Outline each Plasmodium malariae-infected red blood cell.
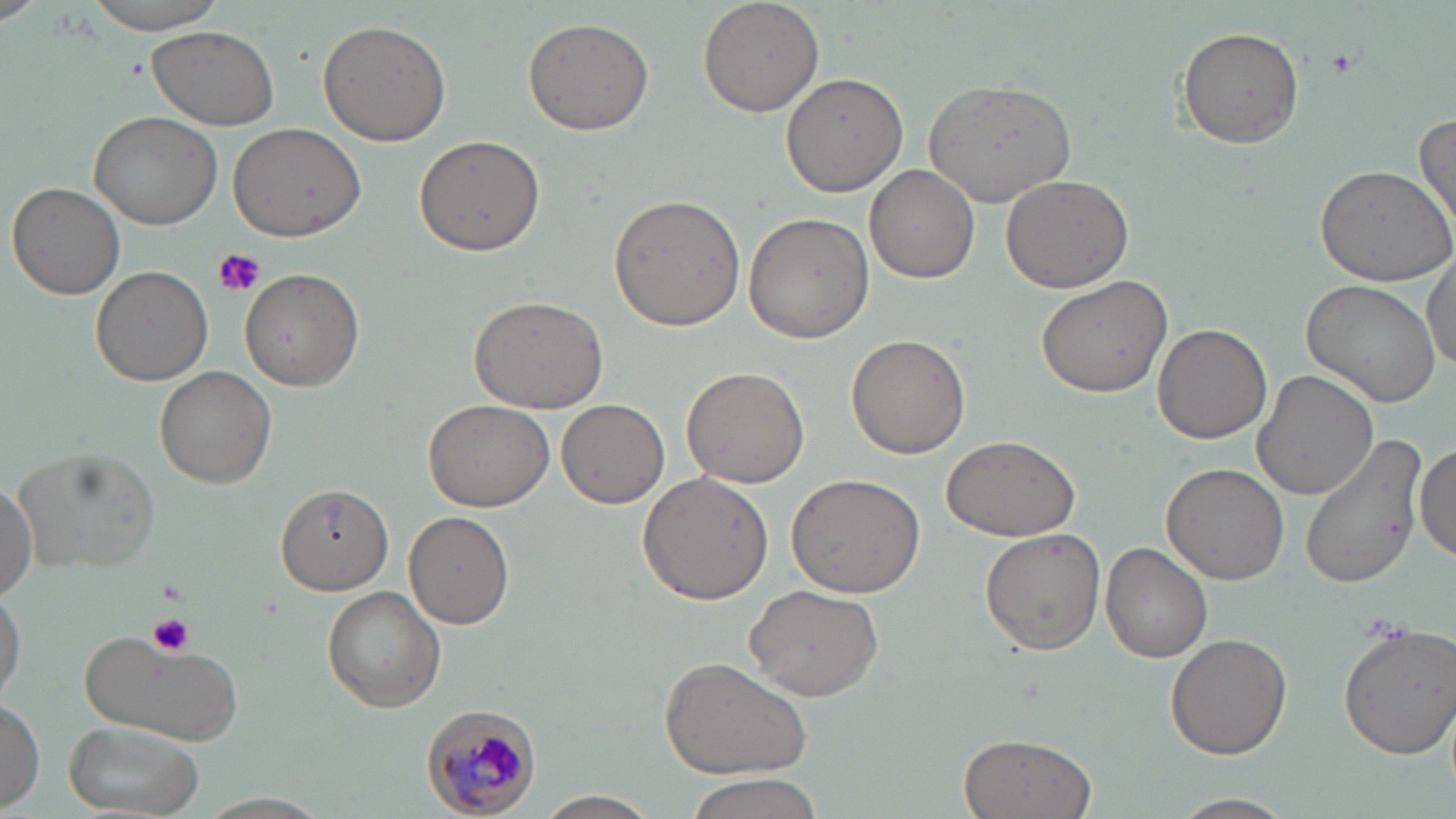
Approximate bounding boxes as [x1, y1, x2, y2] in pixels.
Plasmodium malariae-infected red blood cells: [421, 707, 544, 818].

Uninfected red blood cell locations: [79, 0, 231, 34], [697, 0, 825, 116], [521, 17, 655, 136], [318, 19, 451, 146], [146, 26, 281, 130], [1177, 27, 1304, 149], [782, 70, 909, 197], [924, 79, 1080, 205], [89, 108, 224, 228], [1412, 111, 1456, 230], [228, 120, 365, 243], [412, 135, 546, 258], [1314, 161, 1456, 286], [865, 164, 979, 284], [999, 172, 1133, 294], [7, 181, 125, 299], [608, 194, 746, 331], [744, 211, 874, 343], [1423, 253, 1456, 370], [90, 264, 212, 386], [239, 267, 364, 390], [1034, 275, 1172, 399], [1303, 280, 1443, 408], [468, 290, 611, 413], [1152, 324, 1272, 444], [846, 334, 969, 459], [154, 365, 277, 489], [680, 365, 810, 488], [1252, 369, 1378, 501], [557, 399, 670, 509], [422, 400, 553, 511], [940, 434, 1080, 542], [1300, 438, 1426, 589], [1411, 440, 1455, 564], [18, 448, 160, 573], [1161, 462, 1290, 586], [637, 471, 773, 606], [786, 473, 925, 599], [0, 477, 36, 598], [274, 484, 394, 595], [405, 510, 514, 629], [980, 529, 1107, 654], [1101, 540, 1213, 663], [743, 583, 884, 701], [321, 585, 447, 713], [0, 588, 26, 702], [1337, 621, 1456, 760], [76, 630, 243, 748], [1166, 631, 1293, 759], [659, 655, 814, 780], [1, 698, 43, 810], [60, 719, 207, 819], [957, 732, 1095, 819], [681, 775, 826, 818], [200, 791, 330, 816], [533, 791, 663, 818], [1171, 793, 1296, 819]. Platelet locations: [1323, 47, 1361, 80], [210, 247, 265, 299], [148, 614, 194, 657]. Slide-level diagnosis: Plasmodium malariae. Thin blood film. 1000x magnification. May-Grünwald-Giemsa stain. Image is 1456×819 pixels. Optical microscopy. Single field of view.